Report the malaria status.
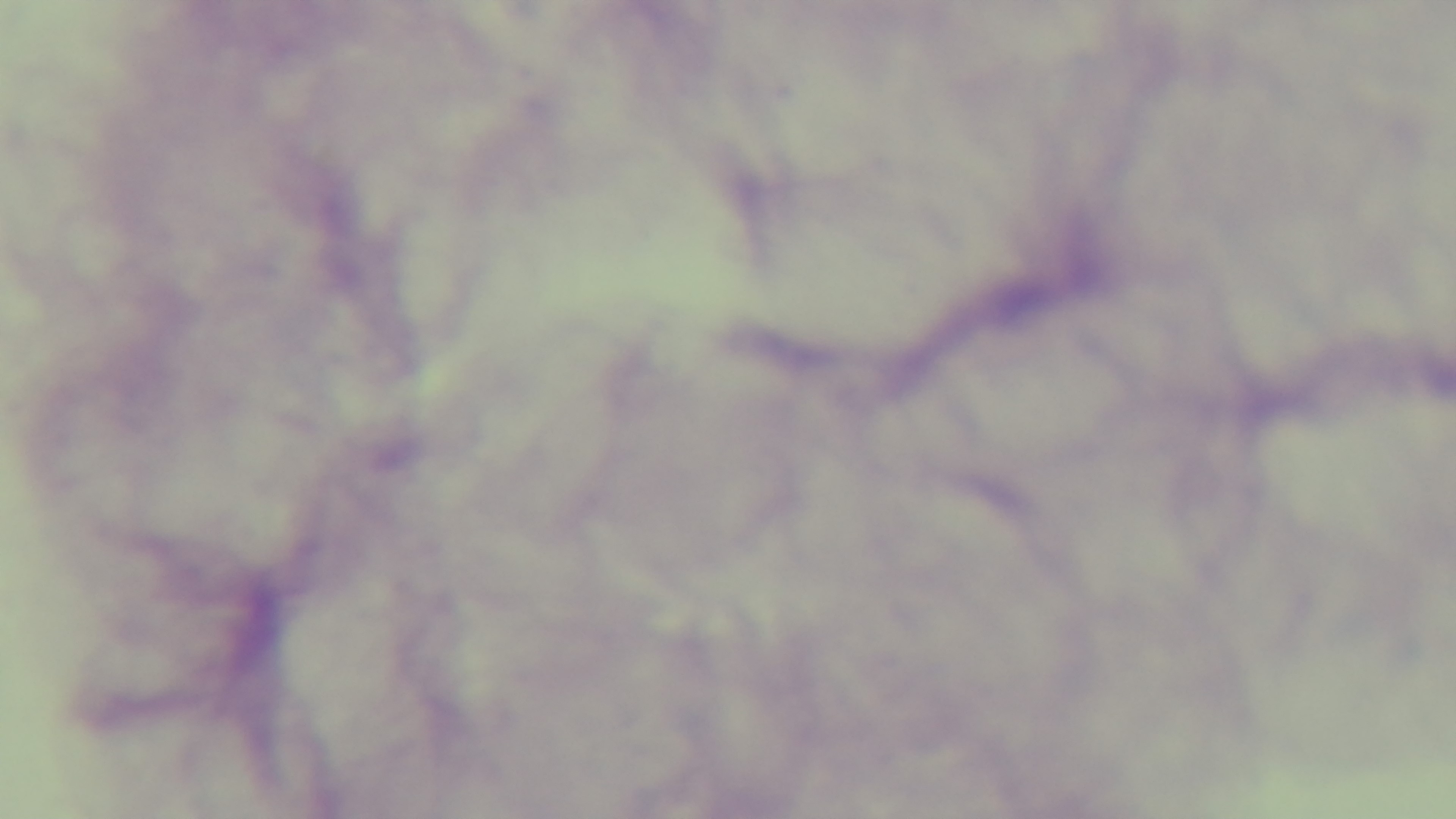

It is uninfected.

{
  "capture": "mounted 4K digital camera",
  "stain": "Giemsa",
  "field_of_view": "one from the slide",
  "modality": "light microscopy",
  "objective": "100x oil immersion",
  "preparation": "thick blood film"
}